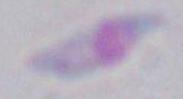

{
  "identification": "Toxoplasma gondii",
  "modality": "micrograph",
  "magnification": "1000x"
}